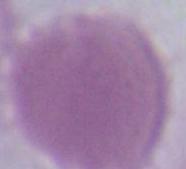

modality = micrograph
magnification = 1000x
identification = erythrocyte